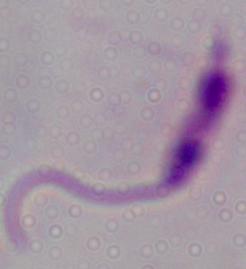

magnification: 1000x
identification: Leishmania
modality: micrograph